Report the malaria status of this cell.
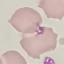
Uninfected.

Cell patch, automatically extracted from a larger field of view and resized to 64 × 64 pixels. Thin blood smear. Acquired by smartphone through the microscope eyepiece. Giemsa-stained preparation.